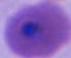
400x or 1000x magnification. Micrograph. A Plasmodium parasite is seen.